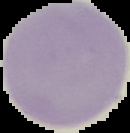 From a thin blood smear. Result: no Plasmodium parasites seen. Segmented cell region on a black background. Image is 130×133 pixels.